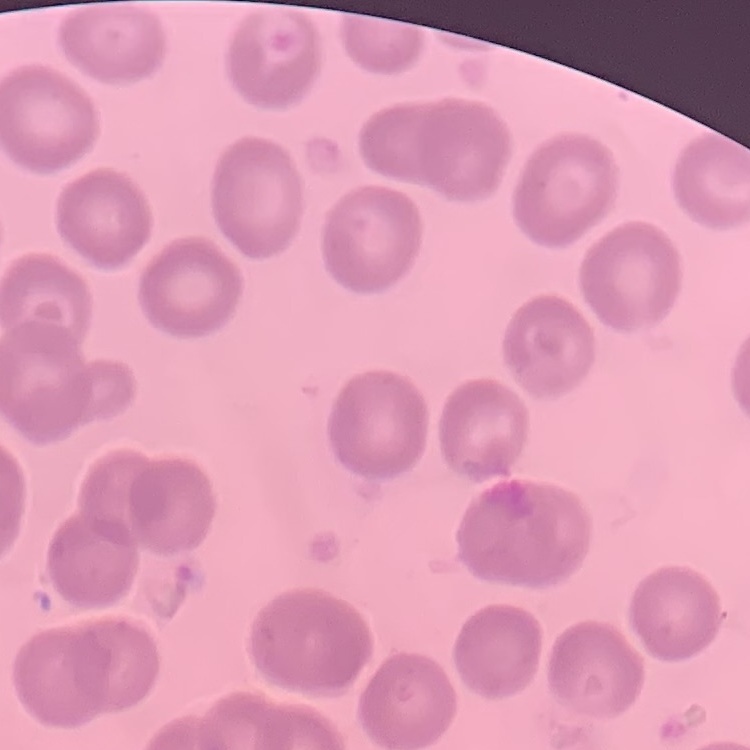
The erythrocytes exhibit no rouleaux formation. Thin blood smear. Stained with either Field's or Giemsa. Square crop of a larger photomicrograph.